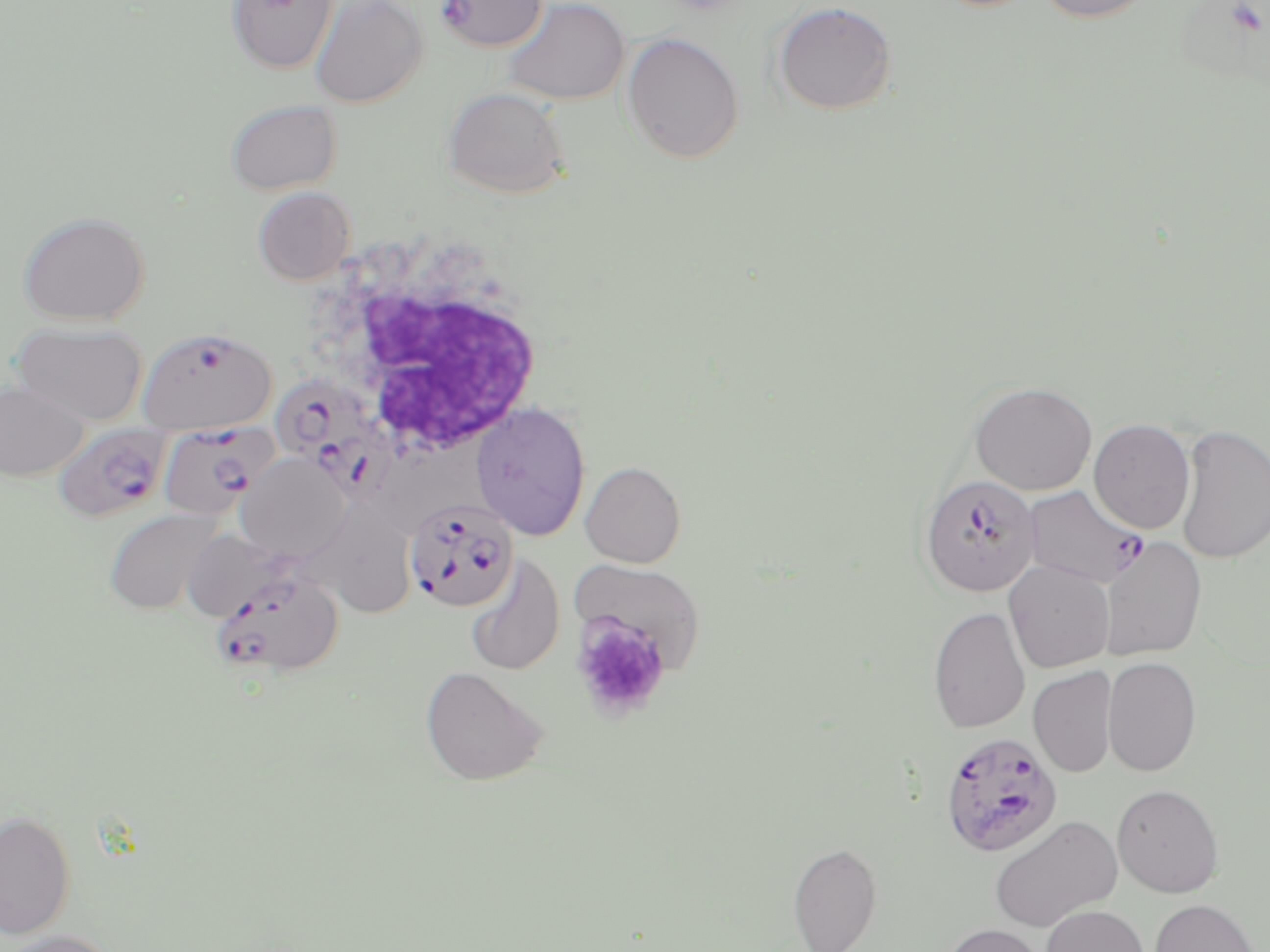

slide_level_diagnosis: Plasmodium falciparum
stain: May-Grünwald-Giemsa
white_blood_cell_locations: 'approximate bounding boxes as (x1,y1)-(x2,y2) corner pairs in pixels: (304,229)-(552,465)'
preparation: thin blood smear
magnification: 1000x
modality: light microscopy
image_size: 1270×952 pixels
uninfected_red_blood_cell_locations_subset: 'approximate bounding boxes as (x1,y1)-(x2,y2) corner pairs in pixels: (226,0)-(338,74), (308,0)-(428,108), (499,0)-(631,105), (771,0)-(898,116), (1031,0)-(1155,24), (621,31)-(744,164), (441,86)-(571,199), (224,99)-(342,195), (252,186)-(356,285), (16,210)-(152,326), (12,321)-(148,426), (0,380)-(89,481), (969,381)-(1097,496), (471,401)-(591,540), (1089,419)-(1196,534), (1174,424)-(1270,565), (236,452)-(351,563), (580,461)-(686,568), (285,500)-(424,613), (103,507)-(224,615), (180,528)-(296,622), (1099,537)-(1208,661), (465,556)-(565,676), (571,560)-(706,672), (1004,561)-(1115,673), (928,606)-(1030,734), (1102,656)-(1202,777), (420,666)-(548,787), (1028,666)-(1117,778), (1112,784)-(1225,898), (0,808)-(77,941), (988,814)-(1123,932), (788,841)-(883,951), (1148,899)-(1262,952), (1040,904)-(1149,952), (940,923)-(1050,952), (0,929)-(121,952)'
plasmodium_falciparum_infected_red_blood_cell_locations_subset: 'approximate bounding boxes as (x1,y1)-(x2,y2) corner pairs in pixels: (435,0)-(547,53), (269,377)-(402,501), (52,422)-(172,523), (156,422)-(273,521), (919,474)-(1040,597), (1022,485)-(1149,588), (405,497)-(520,612), (209,570)-(343,678), (940,731)-(1063,857)'
field_of_view: single
platelet_locations: 'approximate bounding boxes as (x1,y1)-(x2,y2) corner pairs in pixels: (570,613)-(671,721)'